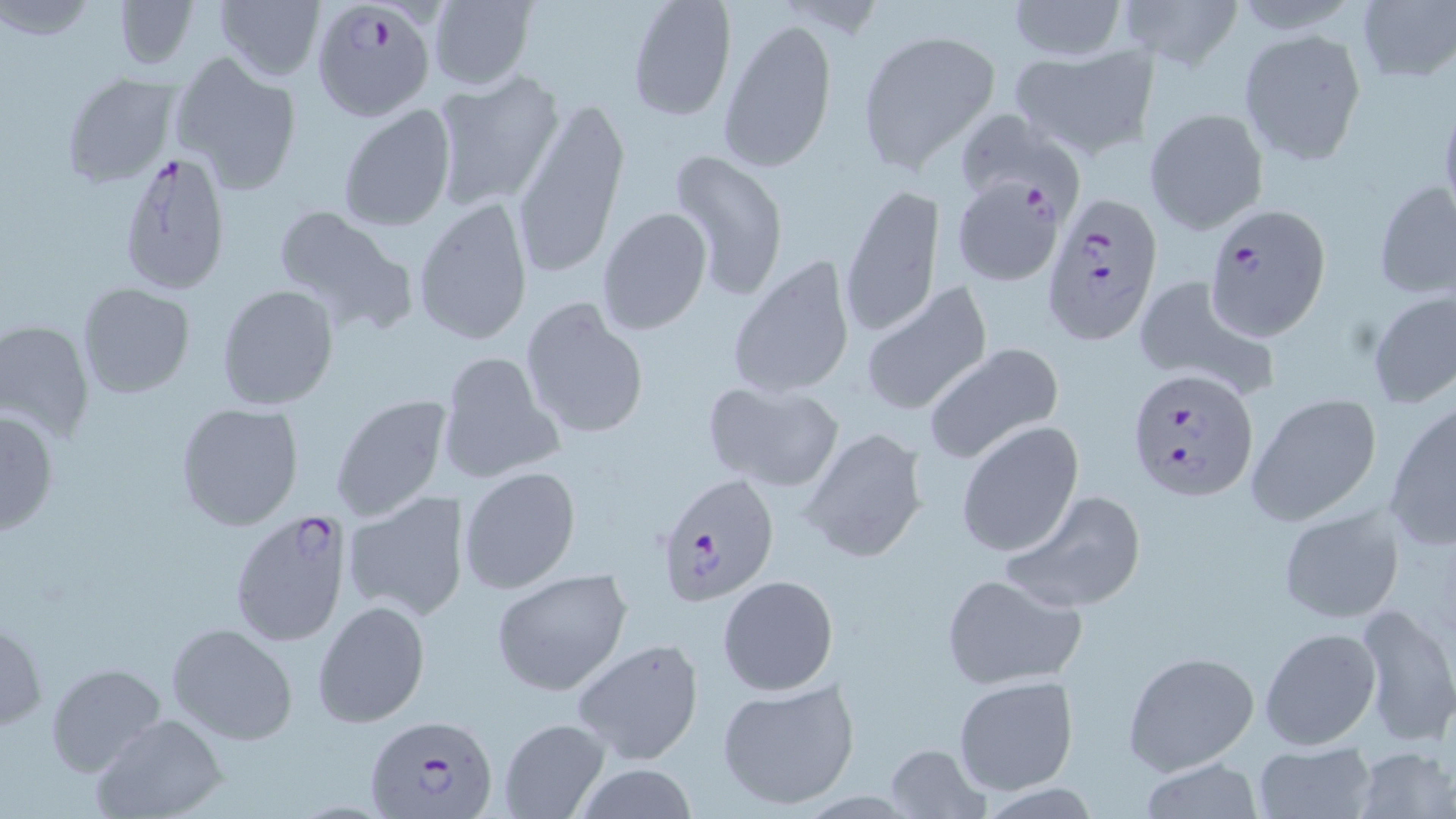
Summary:
  - Coordinate format: approximate bounding boxes as (x1,y1)-(x2,y2) corner pairs in pixels
  - Plasmodium falciparum-infected red blood cell locations: (310,1)-(438,121), (116,149)-(235,296), (951,175)-(1067,285), (1040,193)-(1160,346), (1201,204)-(1329,341), (1124,368)-(1257,502), (657,473)-(780,607), (230,509)-(353,650), (363,715)-(497,817)
  - Uninfected red blood cell locations: (113,0)-(197,72), (1005,0)-(1130,61), (1119,0)-(1241,68), (214,1)-(325,83), (427,1)-(536,91), (625,1)-(736,122), (1352,1)-(1456,87), (719,16)-(837,174), (1238,27)-(1368,166), (857,30)-(1001,171), (1009,45)-(1155,161), (171,50)-(303,196), (60,70)-(180,188), (433,71)-(564,209), (513,98)-(627,274), (338,103)-(457,231), (1144,107)-(1269,235), (951,109)-(1083,212), (666,150)-(790,302), (1371,178)-(1455,300), (842,181)-(942,338), (412,196)-(534,347), (270,203)-(412,328), (596,207)-(712,334), (730,253)-(855,401), (1130,273)-(1278,400), (77,282)-(196,399), (217,284)-(339,411), (856,284)-(992,418), (1365,290)-(1456,411), (520,296)-(650,441), (0,319)-(96,442), (920,342)-(1064,465), (439,350)-(563,484), (702,379)-(844,492), (1245,390)-(1384,527), (329,394)-(450,522), (174,402)-(304,532), (1385,403)-(1456,550), (1,407)-(61,538), (957,421)-(1083,559), (798,425)-(927,562), (458,464)-(581,594), (999,487)-(1148,614), (342,490)-(467,621), (1277,506)-(1405,624), (489,569)-(634,694), (939,571)-(1089,690), (717,573)-(840,696), (312,599)-(431,729), (1352,600)-(1455,746), (0,618)-(46,732), (165,622)-(297,745), (1258,626)-(1380,751), (572,636)-(706,766), (1121,650)-(1259,775), (44,662)-(166,778), (952,675)-(1078,796), (716,677)-(862,812), (92,714)-(228,819), (496,717)-(612,818), (1250,739)-(1379,819), (884,742)-(989,818), (1353,745)-(1455,819), (1134,756)-(1267,819)
  - Slide-level diagnosis: Plasmodium falciparum
  - Modality: optical microscopy
  - Preparation: thin blood film
  - Image size: 1456×819 pixels
  - Stain: May-Grünwald-Giemsa
  - Magnification: 1000x
  - Field of view: single